Identify the preparation type.
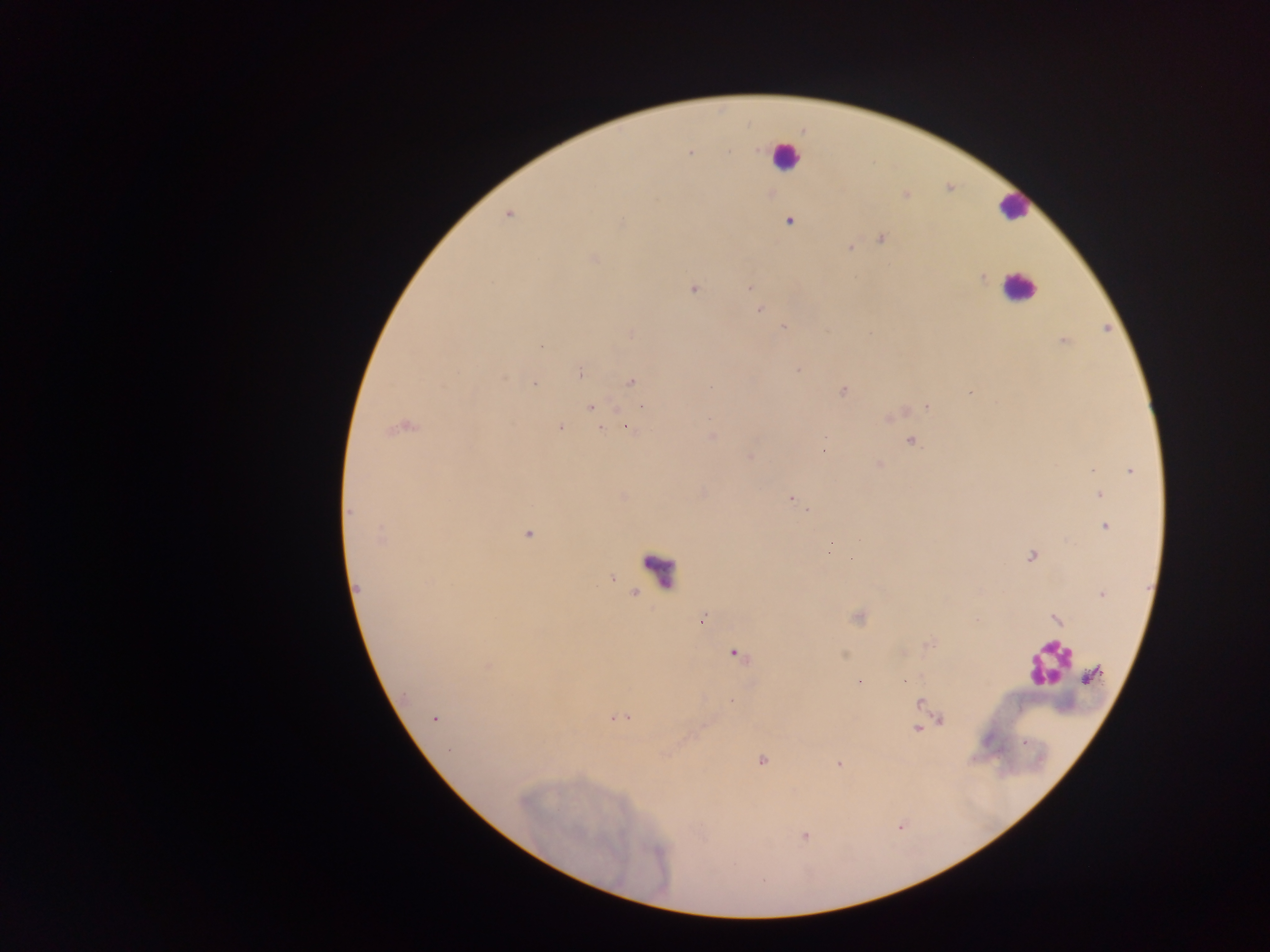
This is a thick smear.

{
  "image_size": "1270×952 pixels",
  "plasmodium_parasite_locations": "approximate centers as [x, y] in pixels: [758, 149], [691, 151], [728, 152], [508, 215], [789, 221], [621, 223], [882, 239], [850, 247], [593, 258], [982, 278], [748, 287], [693, 289], [759, 309], [783, 327], [1064, 341], [541, 346], [798, 370], [581, 372], [504, 379], [632, 382], [534, 383], [843, 390], [591, 406], [926, 406], [642, 407], [402, 427], [628, 427], [560, 428], [600, 428], [712, 436], [826, 437], [911, 441], [824, 450], [750, 458], [879, 465], [1092, 470], [1130, 470], [1099, 495], [791, 498], [808, 510], [350, 512], [1105, 526], [527, 534], [381, 537], [860, 540], [1031, 557], [851, 558], [358, 588], [1101, 594], [701, 620], [1057, 620], [929, 643], [735, 654], [487, 666], [1090, 676], [905, 681], [859, 682], [920, 703], [619, 718], [436, 719], [941, 720], [934, 723], [917, 728], [762, 761], [838, 764], [804, 836]",
  "country": "Ghana",
  "leukocyte_locations": "approximate centers as [x, y] in pixels: [784, 157], [1013, 207], [1018, 287], [654, 568], [1047, 663]",
  "capture": "mobile-phone photograph through a microscope",
  "field_of_view": "single"
}